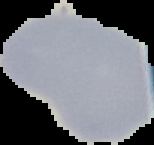
image type = segmented cell region with the area outside set to black
preparation = thin blood smear
image size = 154×145 pixels
result = negative for Plasmodium parasites